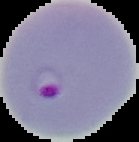

image type = segmented cell region with the area outside set to black
preparation = thin blood smear
malaria status = parasitized
image size = 139×142 pixels